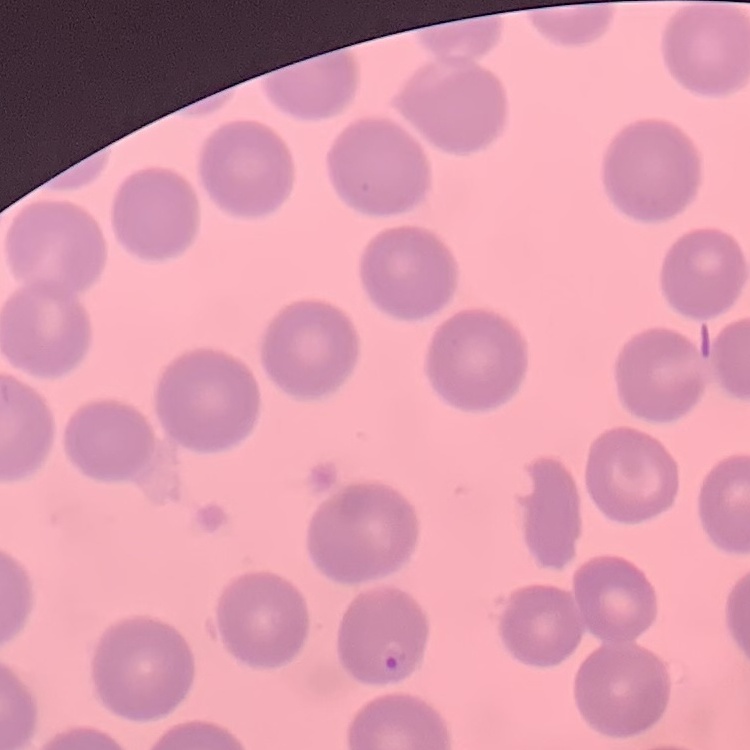
The red blood cells exhibit no rouleaux formation. Thin blood smear. One tile cut from a larger photomicrograph. Field's or Giemsa stain.